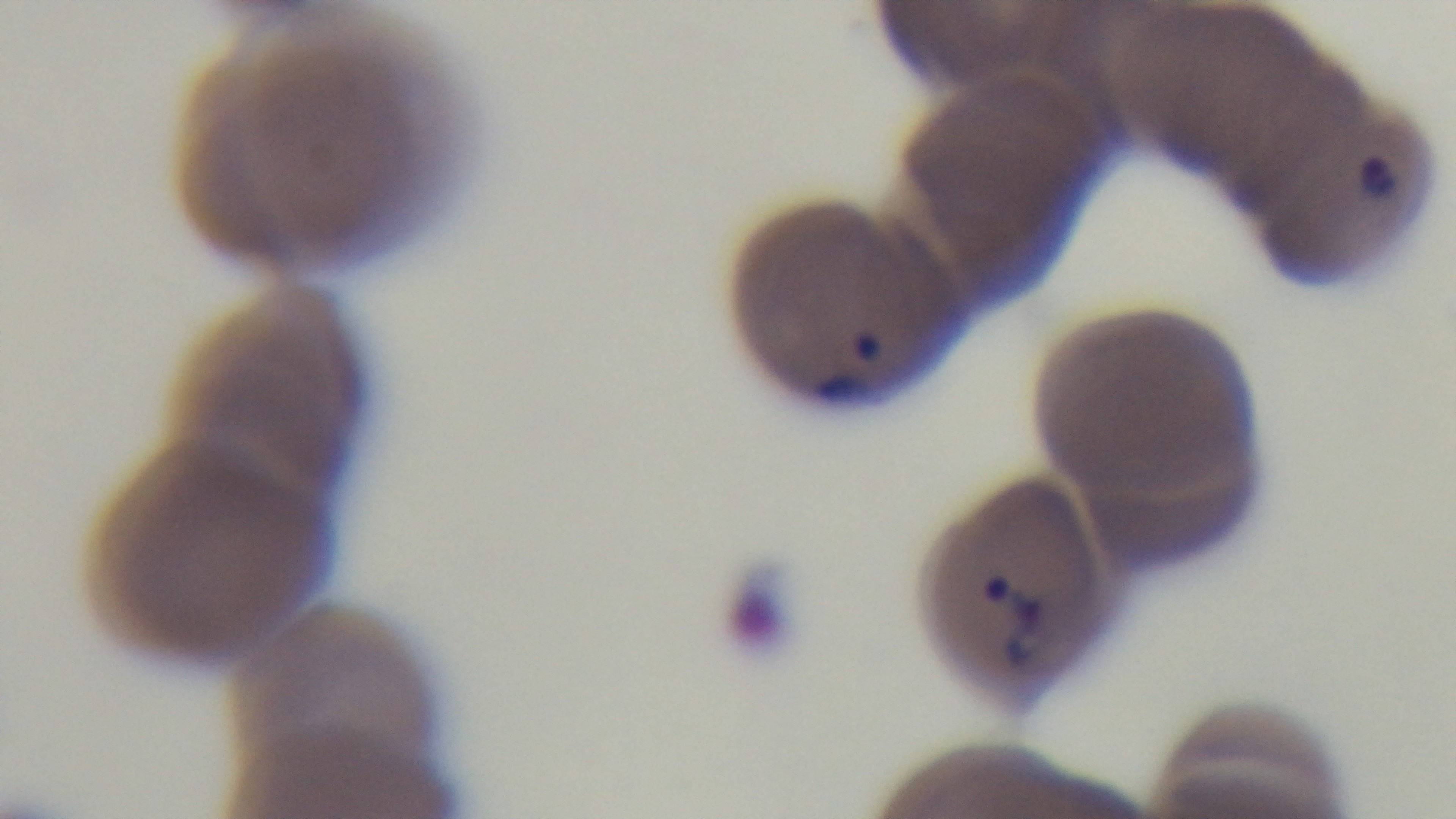

Summary:
  - Capture: mounted 4K digital camera
  - Preparation: thin smear
  - Field of view: one from the slide
  - Malaria status: positive
  - Objective: 100x oil immersion
  - Stain: Giemsa
  - Modality: light microscopy